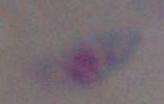
identification: Toxoplasma gondii
modality: micrograph
magnification: 1000x